Locate every P. falciparum parasite and identify its life-cycle stage.
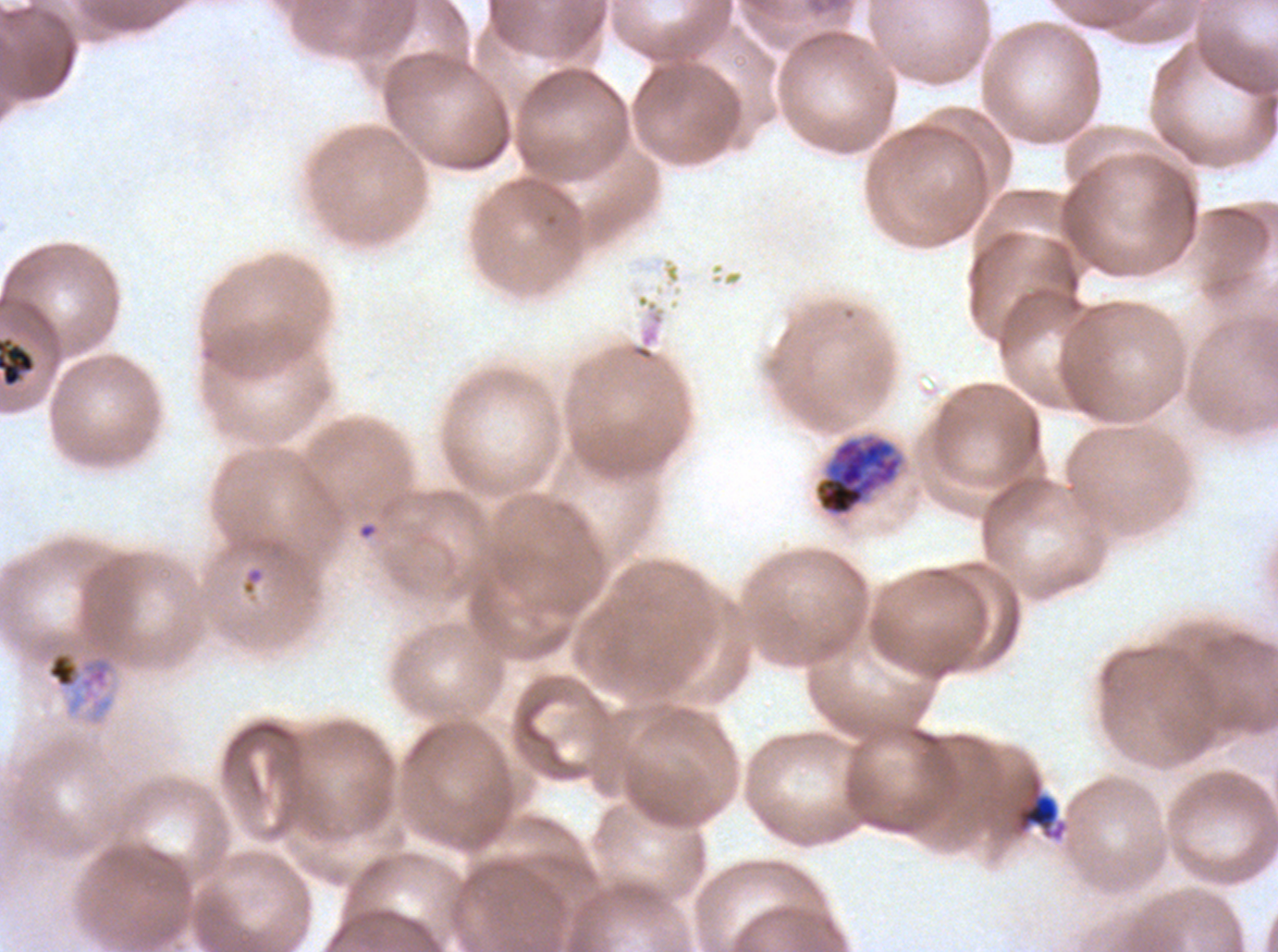

Approximate bounding rectangles given as corner coordinates in pixels from the top-left.
Late-ring/early-trophozoite forms: (x1=1014, y1=778, x2=1067, y2=841).
Late trophozoites: (x1=45, y1=650, x2=114, y2=701).
Early schizonts: (x1=814, y1=434, x2=903, y2=517).
No rings, mid trophozoites, late schizonts, segmenters, or gametocytes observed.

Debris locations: (x1=0, y1=336, x2=35, y2=387). Life-cycle stages observed: late-ring/early-trophozoite, late trophozoite, early schizont. One sub-image of a larger composite. Thin blood film. Ex-vivo P. falciparum culture from a patient in The Gambia, grown for 24 to 48 hours. Image is 1278×952 pixels. Giemsa-stained preparation.